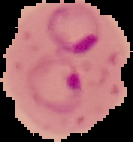

image size = 133×142 pixels
result = malaria parasites detected
preparation = thin blood film
image type = cell region segmented out of the field of view; surrounding area masked to black